Evaluate for Plasmodium parasites.
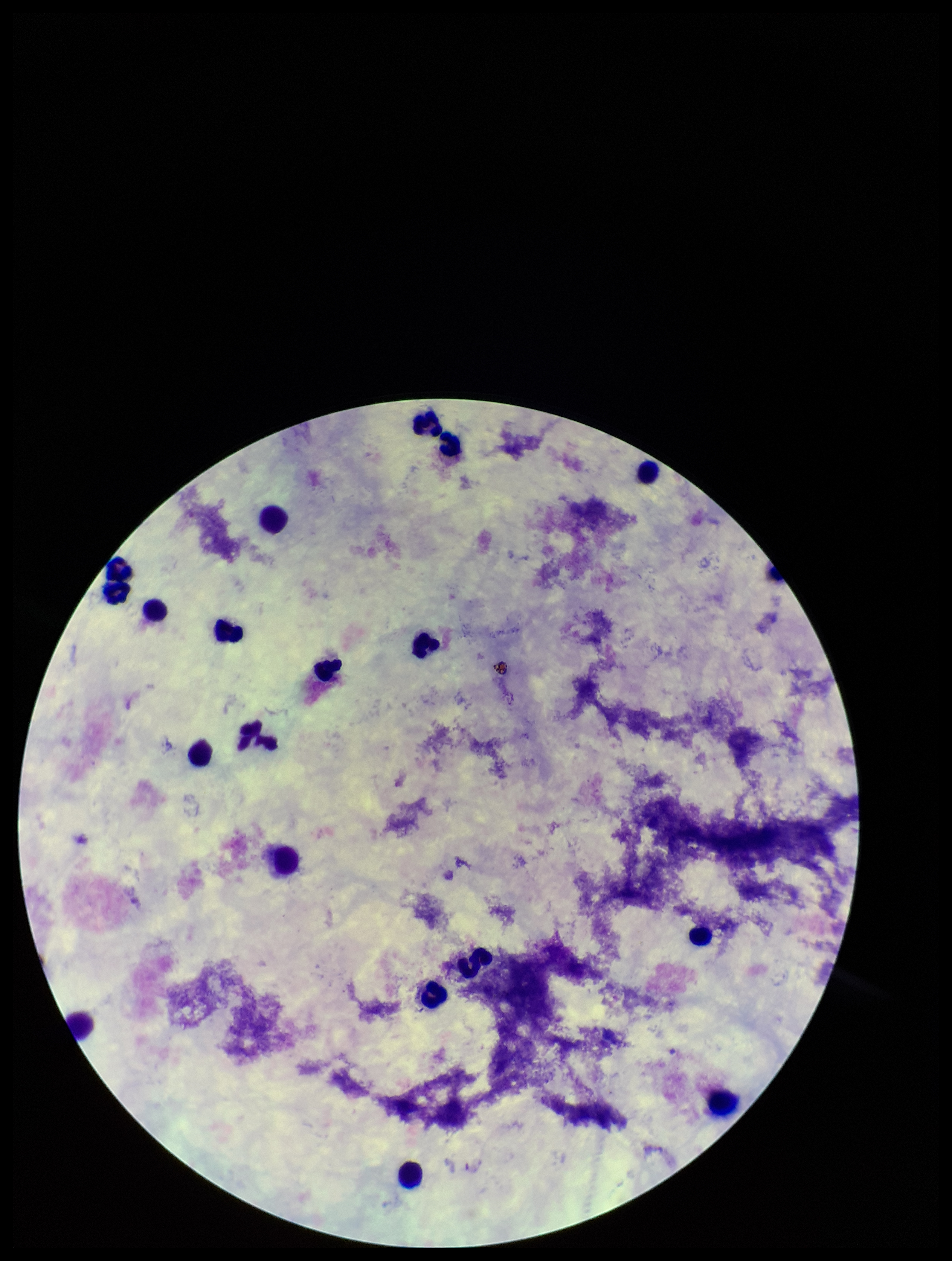
None identified.

stain = Giemsa
leukocyte count = 18
image size = 952×1261 pixels
field of view = single
capture = smartphone photograph through the microscope eyepiece
patient malaria status = negative
parasite count = 0
preparation = thick